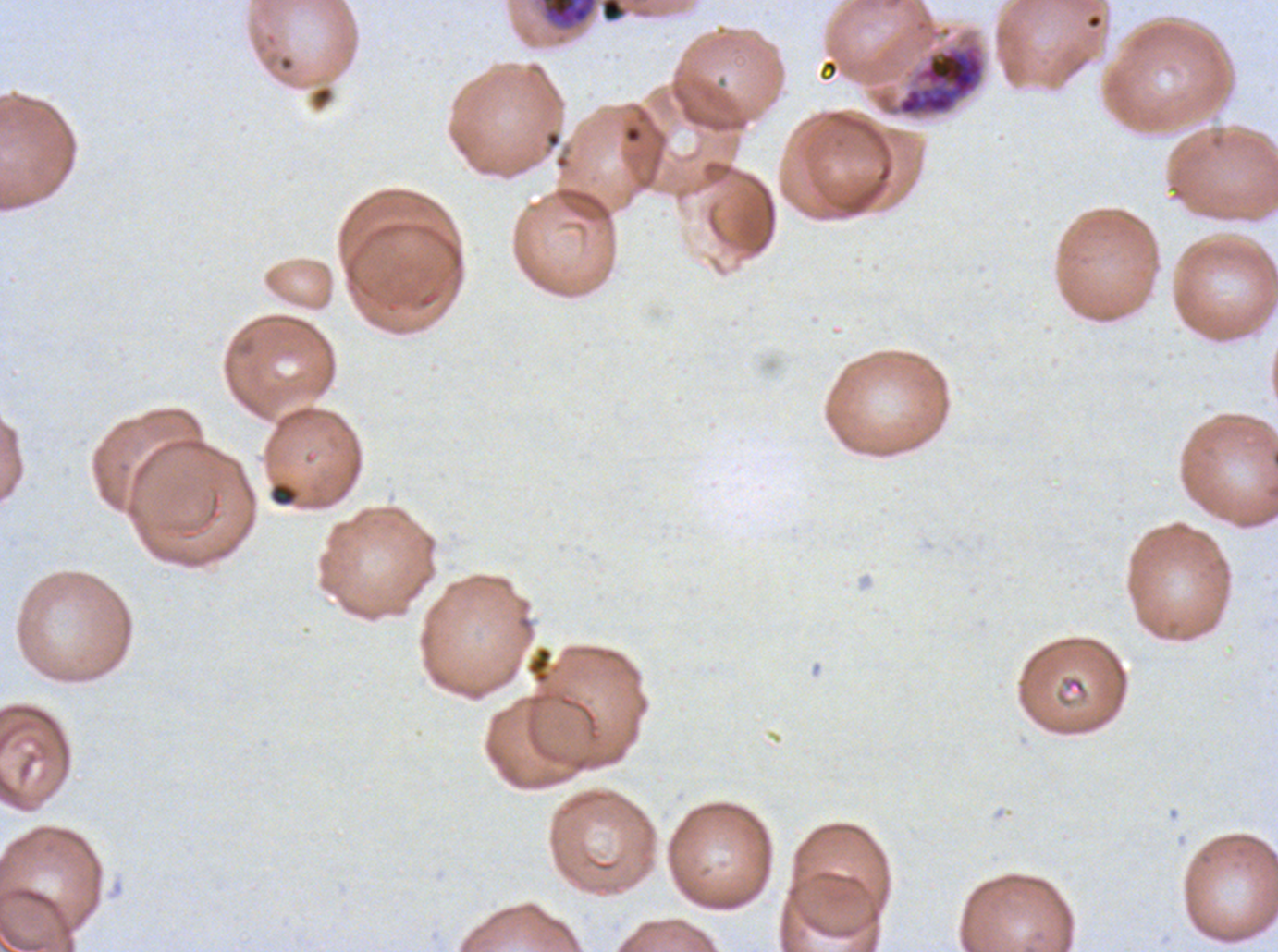

Approximate bounding boxes as {x1, y1, x2, y2} in pixels. Debris locations: {269, 482, 298, 507}, {525, 645, 554, 685}. Early schizont locations: {871, 29, 988, 121}. Late trophozoite locations: {540, 0, 597, 28}. Thin blood smear. Giemsa stain. A sub-image separated from a larger composite. P. falciparum from a patient in The Gambia, cultured ex vivo for 24 to 48 hours. Image is 1278×952 pixels. Life-cycle stages observed: late trophozoite, early schizont.